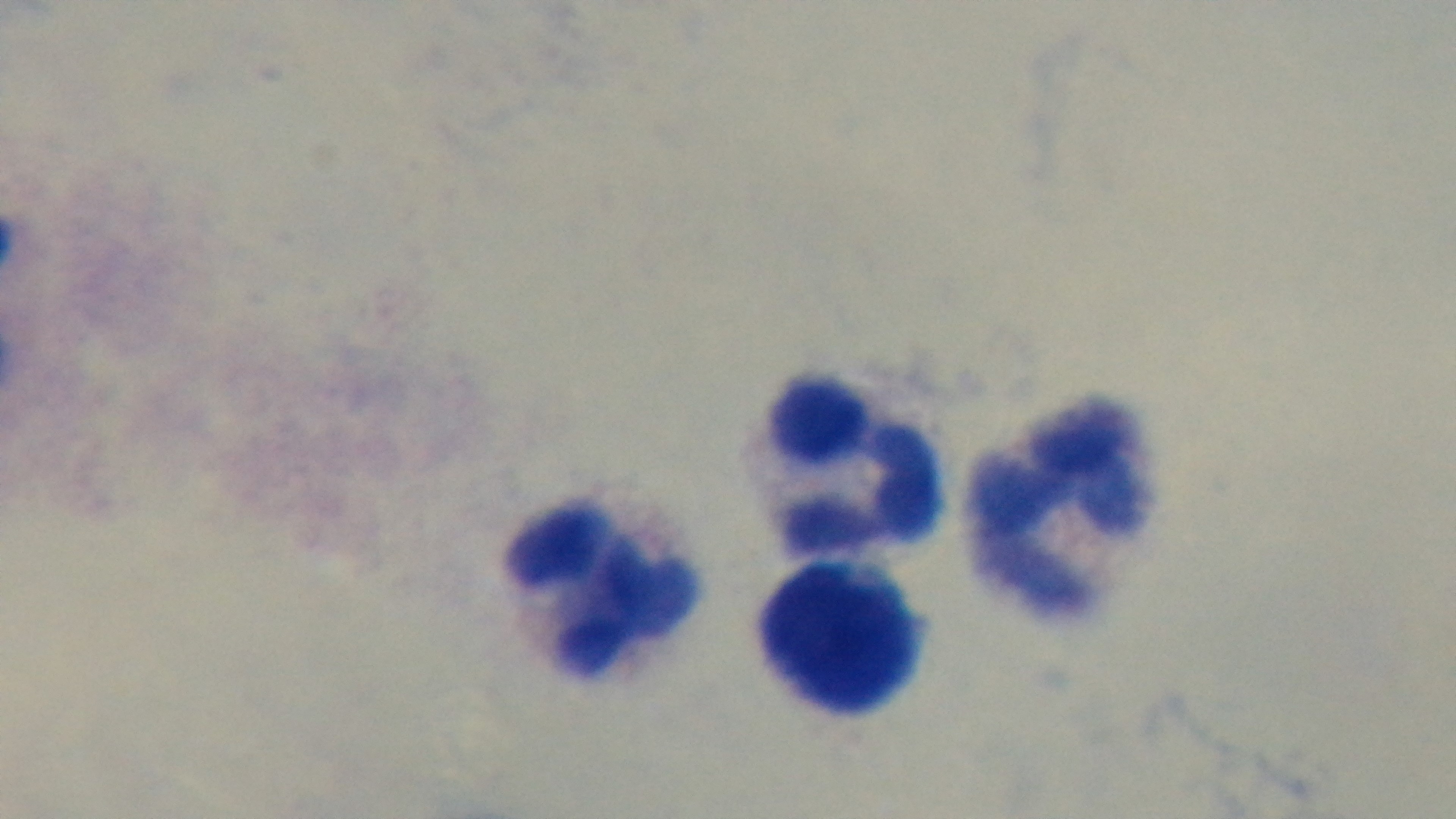

objective: 100x oil immersion
capture: mounted 4K digital camera
malaria_status: negative
modality: light microscopy
stain: Giemsa
field_of_view: one from the slide
preparation: thick smear